Classify this cell by malaria status.
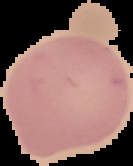
Uninfected.

preparation = thin blood film
image type = segmented cell region on a black background
image size = 133×166 pixels